Evaluate for Plasmodium parasites.
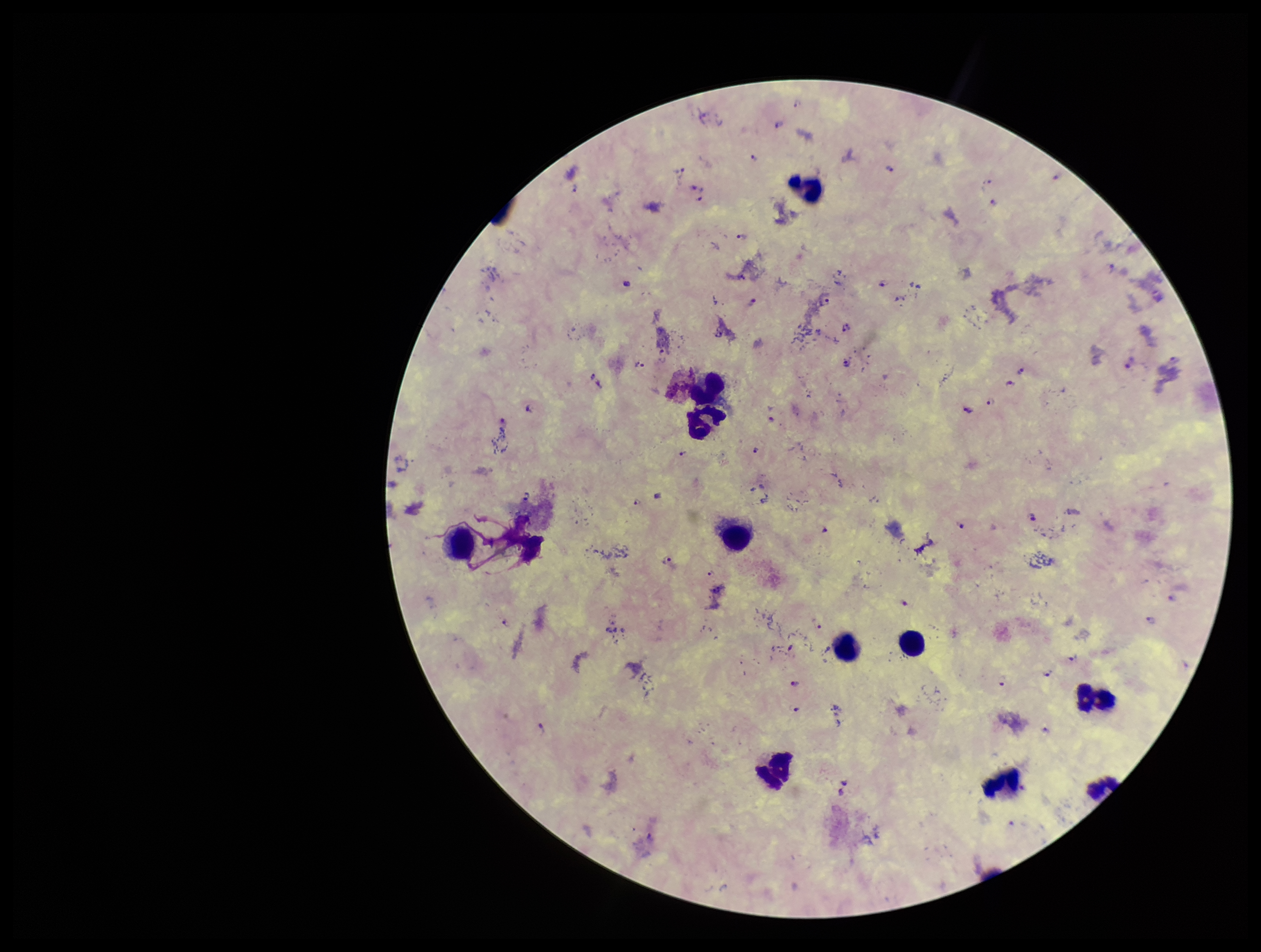

Detected.

Species reported for this patient: Plasmodium falciparum. Image is 1261×952 pixels. Patient malaria status: infected. Stained with Giemsa. Parasite count: 40. Leukocyte count: 11. Smartphone photograph taken through the eyepiece of a microscope. One field from this slide. Preparation: thick blood smear.